Assess the morphology of the red blood cells.
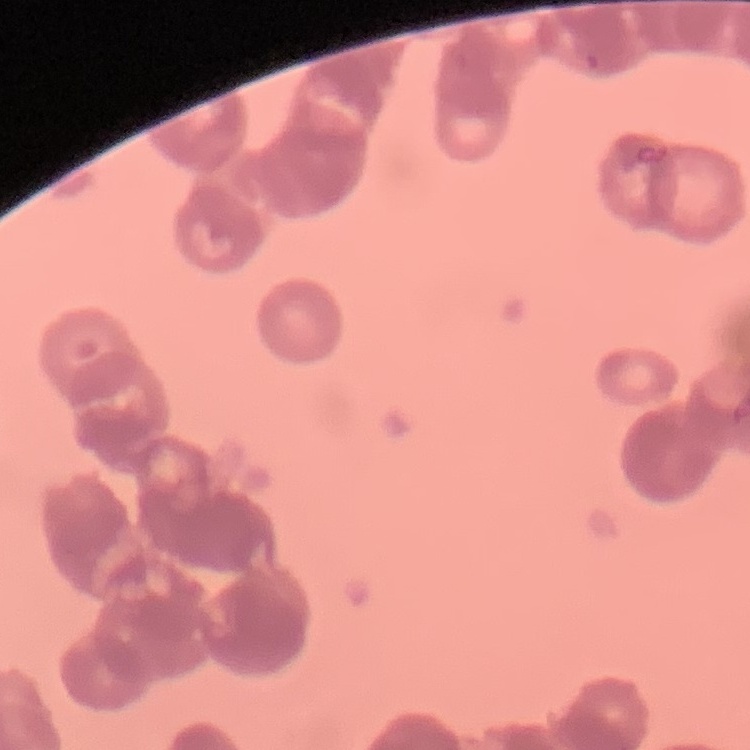
Rouleaux formation.

Summary:
  - Stain: Field's or Giemsa
  - Image type: one tile cut from a larger photomicrograph
  - Preparation: thin peripheral smear